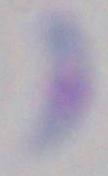
Summary:
  - Magnification: 1000x
  - Identification: Toxoplasma gondii
  - Modality: photomicrograph